Outline each blood parasite and name the species.
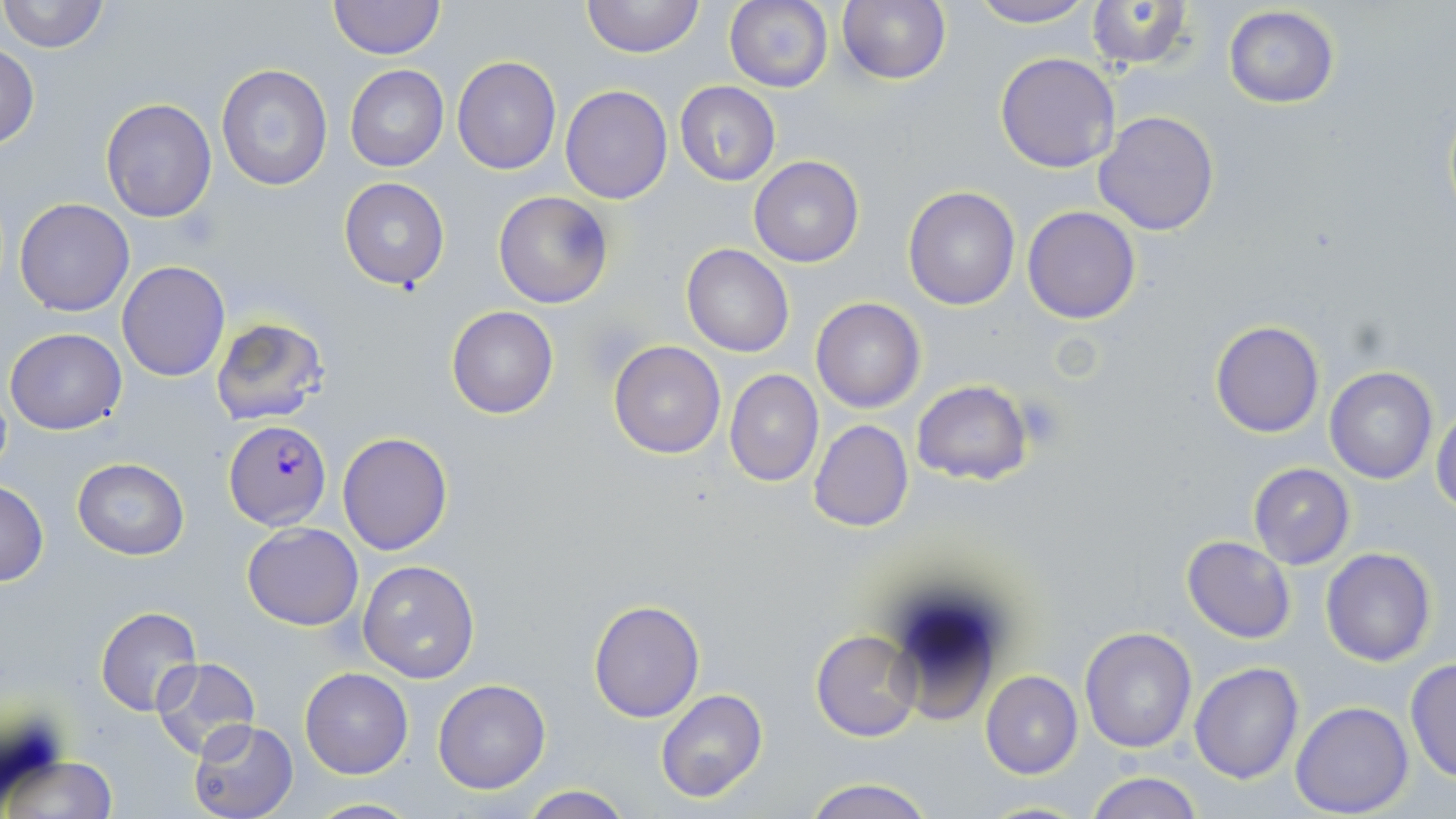
Approximate bounding boxes as [x1, y1, x2, y2] in pixels.
Plasmodium falciparum-infected red blood cells: [224, 420, 331, 529].
No Plasmodium ovale, Plasmodium malariae, Plasmodium vivax, Babesia divergens, or Trypanosoma brucei observed.

slide-level diagnosis = Plasmodium falciparum
image size = 1456×819 pixels
modality = optical microscopy
magnification = 1000x
stain = May-Grünwald-Giemsa
uninfected red blood cell locations = approximate bounding boxes as [x1, y1, x2, y2] in pixels: [1, 0, 112, 54], [328, 0, 444, 60], [581, 0, 704, 59], [725, 0, 833, 92], [965, 0, 1096, 27], [1082, 0, 1197, 71], [834, 1, 952, 86], [1222, 5, 1341, 109], [0, 44, 39, 149], [995, 51, 1121, 173], [452, 55, 562, 174], [215, 62, 335, 192], [345, 66, 449, 172], [675, 80, 780, 185], [560, 84, 672, 204], [101, 98, 216, 222], [1093, 110, 1221, 235], [749, 156, 863, 268], [339, 177, 450, 292], [902, 186, 1022, 310], [493, 191, 614, 309], [13, 198, 135, 317], [1022, 205, 1141, 325], [681, 244, 794, 359], [117, 260, 231, 382], [811, 297, 926, 413], [446, 306, 560, 419], [210, 316, 330, 425], [1210, 319, 1326, 438], [4, 326, 128, 435], [608, 340, 725, 458], [1324, 366, 1437, 484], [724, 370, 823, 488], [913, 380, 1031, 485], [1432, 405, 1456, 514], [807, 419, 914, 532], [337, 430, 453, 556], [72, 458, 191, 560], [1247, 462, 1354, 570], [0, 480, 48, 585], [242, 523, 363, 630], [1182, 534, 1296, 644], [1320, 547, 1437, 666], [357, 559, 482, 683], [589, 597, 705, 722], [94, 606, 202, 716], [1080, 627, 1197, 753], [810, 629, 924, 741], [150, 656, 263, 762], [1404, 658, 1455, 782], [1189, 663, 1304, 783], [301, 668, 414, 778], [981, 671, 1083, 778], [433, 679, 551, 794], [655, 688, 770, 804], [1290, 701, 1414, 818], [189, 719, 300, 819], [5, 752, 118, 819], [1085, 772, 1203, 819], [800, 778, 938, 819], [518, 785, 636, 818], [303, 796, 421, 817], [974, 798, 1095, 818]
preparation = thin blood film
field of view = one of a larger specimen
platelet locations = approximate bounding boxes as [x1, y1, x2, y2] in pixels: [1017, 396, 1067, 450]